Classify this cell by malaria status.
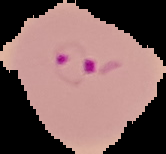
Parasitized.

From a thin blood smear. Cell region segmented out of the field of view; the surrounding area is masked to black. Image is 166×154 pixels.